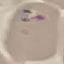 Result: negative for malaria parasites. Automatically extracted cell patch, resized to 64 × 64 pixels. Thin blood film. Giemsa-stained preparation. Photographed with a smartphone camera at the microscope eyepiece.